Report the malaria status of this cell.
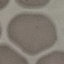
It is uninfected.

stain = Giemsa
preparation = thin blood film
image type = cell patch, automatically extracted from a larger field of view and resized to 64 × 64 pixels
capture = smartphone through the microscope eyepiece